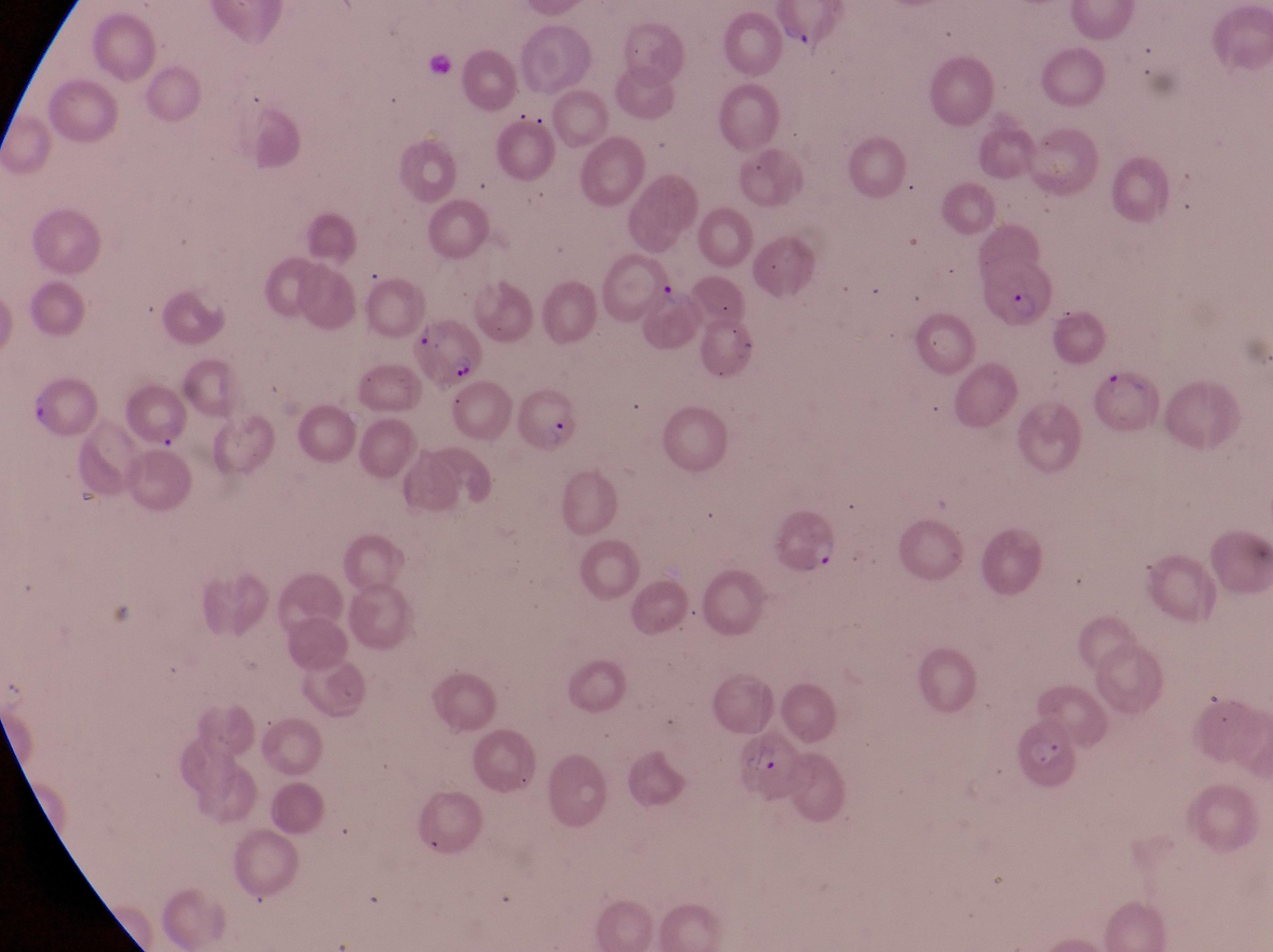
Approximate bounding boxes as (left, top, right, bottom) in pixels. Trophozoite locations: (649, 272, 692, 307). Artifact (platelet-like body, stain precipitate, or debris) locations: (25, 390, 48, 425). Parasitised red blood cell locations: (984, 255, 1056, 335), (414, 322, 484, 397), (514, 387, 579, 457), (771, 510, 838, 577), (732, 727, 806, 801). At a magnification of 1000x. Thin blood smear. Image is 1273×952 pixels. One field of view. Captured by a smartphone held over the eyepiece of an Olympus CX-23 microscope. Collected in Uganda.